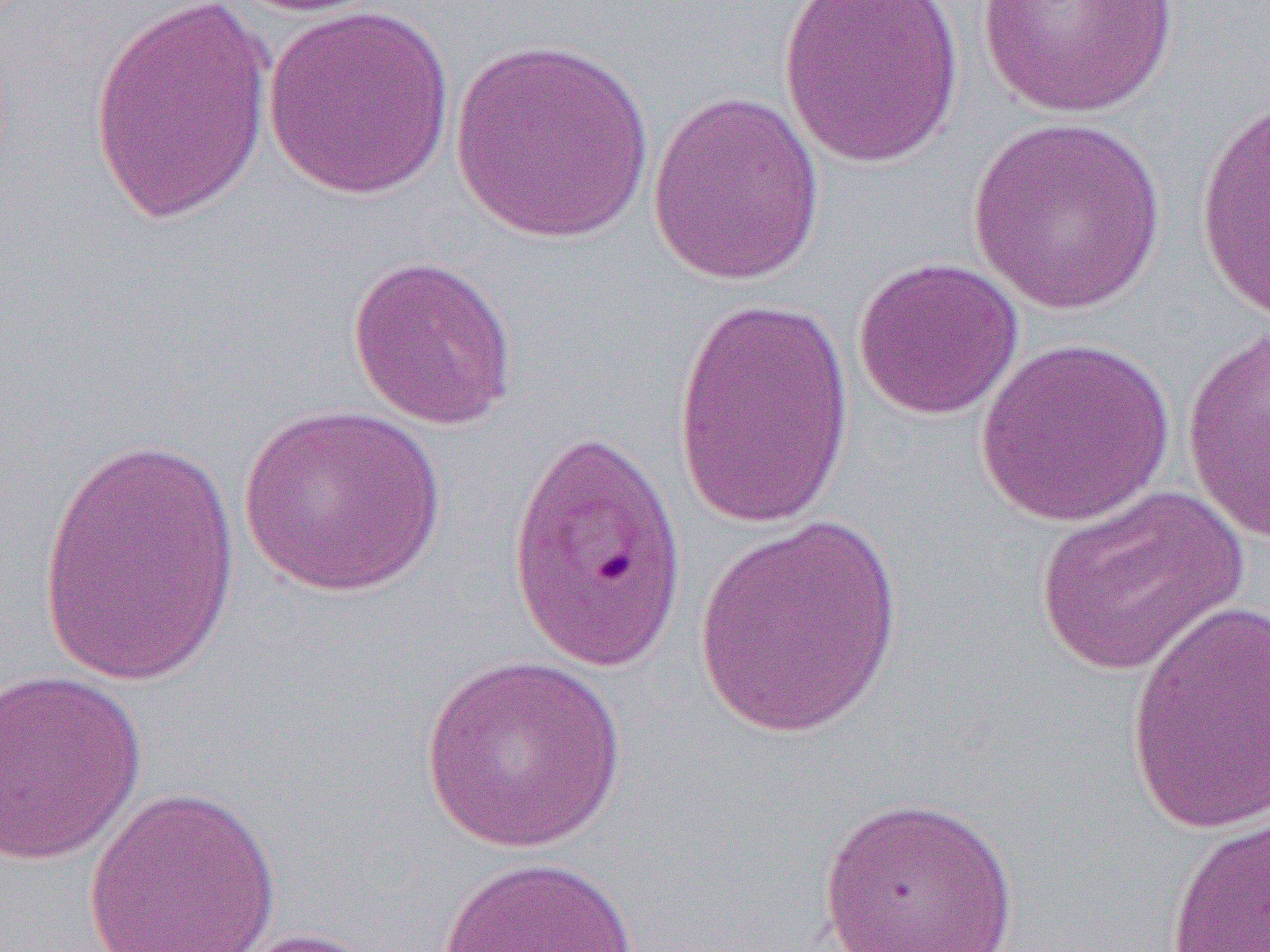

Summary:
  - Coordinate format: approximate bounding boxes as named x1/y1/x2/y2 corners in pixels
  - Uninfected red blood cell locations: (x1=224, y1=0, x2=396, y2=17), (x1=774, y1=0, x2=966, y2=170), (x1=976, y1=0, x2=1179, y2=118), (x1=88, y1=1, x2=275, y2=223), (x1=263, y1=5, x2=455, y2=199), (x1=449, y1=37, x2=656, y2=245), (x1=646, y1=90, x2=825, y2=286), (x1=1195, y1=97, x2=1270, y2=325), (x1=966, y1=116, x2=1169, y2=315), (x1=347, y1=255, x2=519, y2=431), (x1=851, y1=256, x2=1025, y2=421), (x1=670, y1=294, x2=854, y2=535), (x1=1181, y1=324, x2=1270, y2=545), (x1=974, y1=337, x2=1175, y2=528), (x1=236, y1=404, x2=447, y2=599), (x1=505, y1=426, x2=692, y2=676), (x1=34, y1=434, x2=242, y2=689), (x1=1035, y1=484, x2=1247, y2=678), (x1=693, y1=513, x2=908, y2=739), (x1=1123, y1=598, x2=1269, y2=835), (x1=420, y1=654, x2=628, y2=853), (x1=0, y1=670, x2=148, y2=867), (x1=83, y1=785, x2=282, y2=952), (x1=816, y1=795, x2=1021, y2=952), (x1=1163, y1=809, x2=1270, y2=952), (x1=434, y1=856, x2=641, y2=952), (x1=211, y1=926, x2=394, y2=951)
  - Slide-level diagnosis: Plasmodium falciparum
  - Modality: optical microscopy
  - Image size: 1270×952 pixels
  - Magnification: 1000x
  - Field of view: one of a larger specimen
  - Preparation: thin blood smear